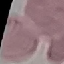
result = no malaria parasites seen
preparation = thin smear
capture = smartphone camera at the microscope eyepiece
stain = Giemsa
image type = automatically extracted cell patch, resized to 64 × 64 pixels